Outline every malaria parasite.
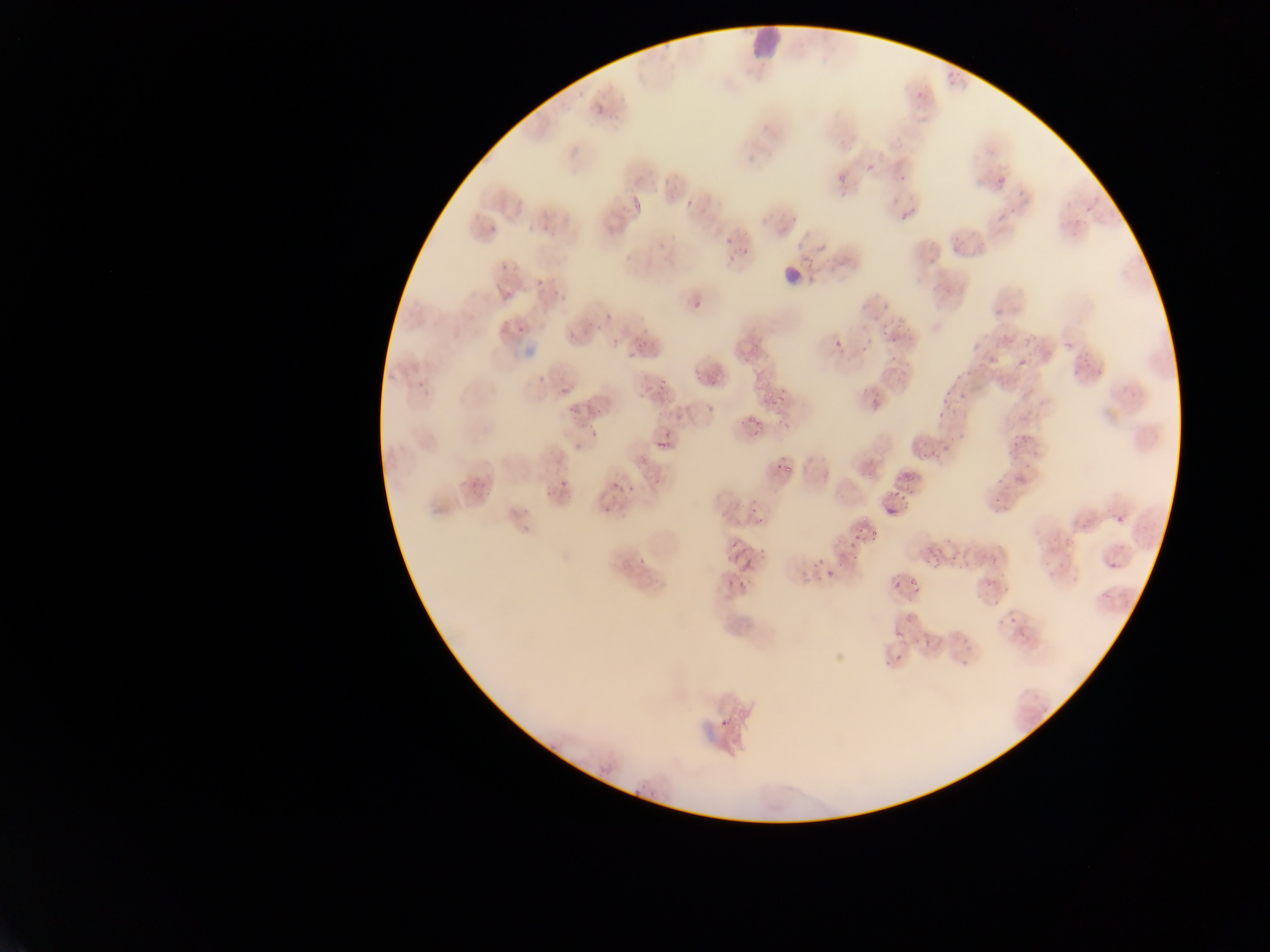

Approximate bounding boxes as (left, top, right, bottom) in pixels.
Malaria parasites: (911, 88, 931, 108), (590, 95, 605, 117), (868, 154, 888, 176), (894, 163, 909, 185), (831, 164, 849, 185), (625, 190, 642, 224), (681, 194, 691, 206), (897, 206, 911, 224), (723, 227, 736, 246), (739, 238, 757, 263), (493, 256, 511, 277), (532, 266, 549, 290), (688, 277, 711, 318), (870, 303, 892, 325), (598, 312, 615, 322), (512, 321, 523, 335), (581, 322, 594, 335), (562, 324, 576, 341), (885, 328, 906, 346), (968, 328, 989, 352), (831, 336, 846, 353), (610, 338, 625, 348), (988, 344, 1002, 366), (1016, 354, 1040, 368), (530, 371, 547, 385), (763, 380, 792, 408), (953, 382, 968, 401), (647, 383, 671, 404), (557, 384, 568, 399), (938, 384, 952, 403), (681, 390, 703, 412), (929, 408, 948, 422), (775, 410, 796, 434), (744, 411, 762, 439), (1004, 420, 1030, 456), (586, 423, 600, 440), (915, 426, 939, 463), (653, 427, 671, 452), (937, 433, 954, 463), (1016, 447, 1040, 476), (905, 455, 919, 474), (774, 460, 793, 478), (553, 467, 574, 492), (991, 476, 1003, 496), (620, 478, 640, 494), (604, 480, 618, 494), (888, 482, 908, 511), (748, 492, 769, 527), (599, 504, 607, 514), (1112, 512, 1128, 529), (849, 526, 876, 545), (729, 537, 747, 563), (634, 549, 652, 568), (807, 551, 829, 572), (740, 555, 758, 576), (822, 569, 844, 586), (909, 569, 924, 591), (887, 575, 907, 598), (723, 577, 734, 593), (982, 594, 998, 608), (1002, 605, 1026, 622), (917, 635, 935, 659), (889, 641, 901, 668), (715, 716, 729, 733).

Summary:
  - Leukocyte locations: (744, 20, 791, 67)
  - Field of view: single
  - Country: Ghana
  - Image size: 1270×952 pixels
  - Preparation: thin blood smear
  - Capture: mobile-phone photograph through a microscope